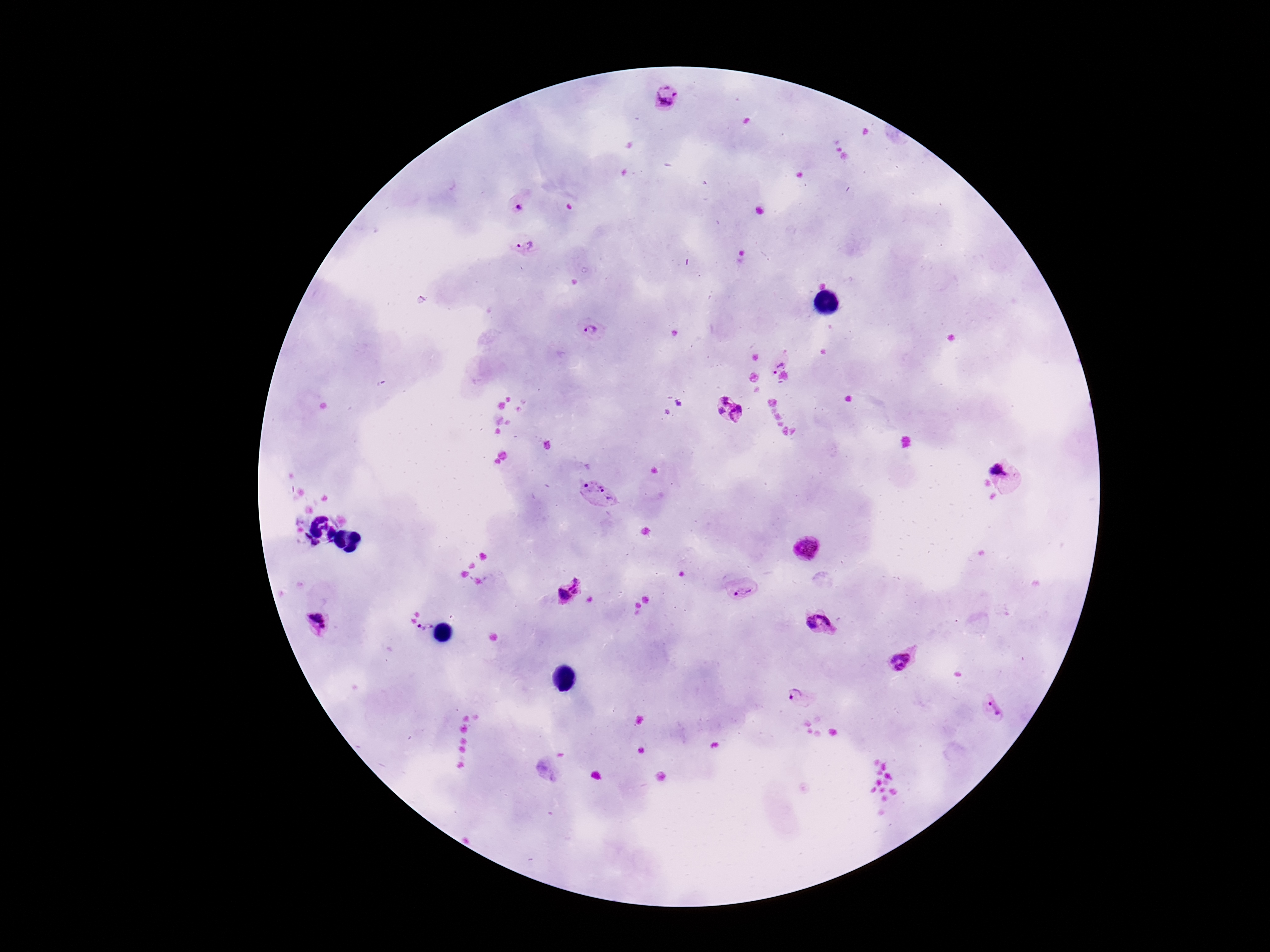
Approximate object centers, in pixels from the top-left corner. Plasmodium parasite locations: (x=669, y=99), (x=522, y=200), (x=521, y=246), (x=594, y=332), (x=777, y=361), (x=730, y=409), (x=1007, y=475), (x=600, y=494), (x=306, y=536), (x=315, y=543), (x=805, y=548), (x=567, y=589), (x=743, y=590), (x=819, y=620), (x=318, y=622), (x=424, y=625), (x=901, y=659), (x=802, y=696), (x=992, y=707). Image is 1270×952 pixels. Photographed through the microscope eyepiece with a smartphone camera. 100x magnification. Thick peripheral-blood smear. Patient malaria status: infected. Single field of view. Giemsa stain.